Assess this cell for malaria.
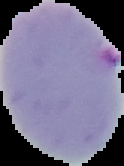

It is parasitized.

preparation = thin blood film
image size = 124×166 pixels
image type = segmented cell region on a black background